Point out each Plasmodium parasite.
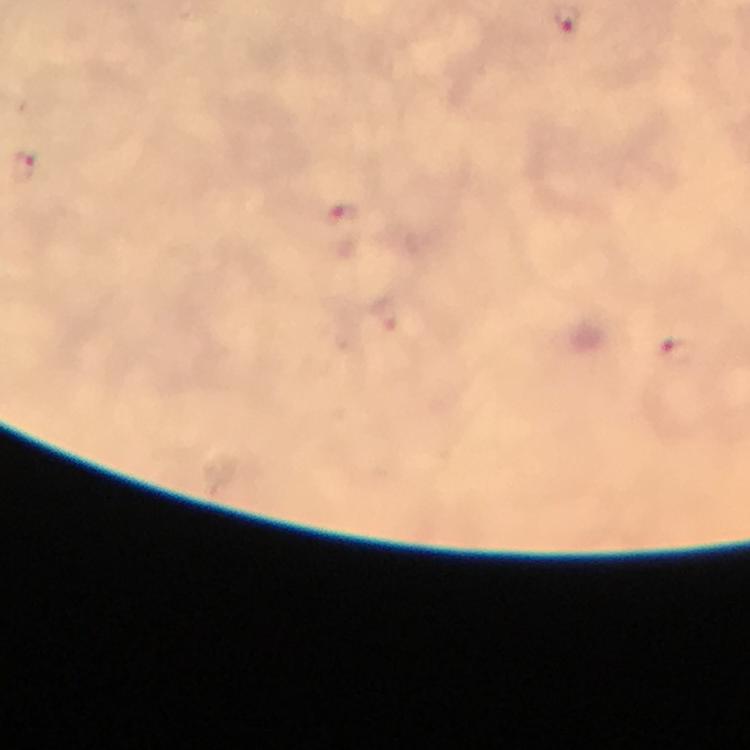

Approximate centers as (x, y) in pixels.
Plasmodium parasites: (25, 164), (341, 212), (676, 350).

Smartphone photograph taken through a microscope. A crop from one field of view. From a diagnostic examination for malaria. Image is 750×750 pixels. Thick blood smear. Giemsa stain. 100x magnification. Immersion oil applied.